Report the malaria status of this cell.
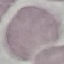
It is uninfected.

Automatically extracted cell patch, resized to 64 × 64 pixels. Thin blood smear. Photographed with a smartphone camera at the microscope eyepiece. Giemsa stain.